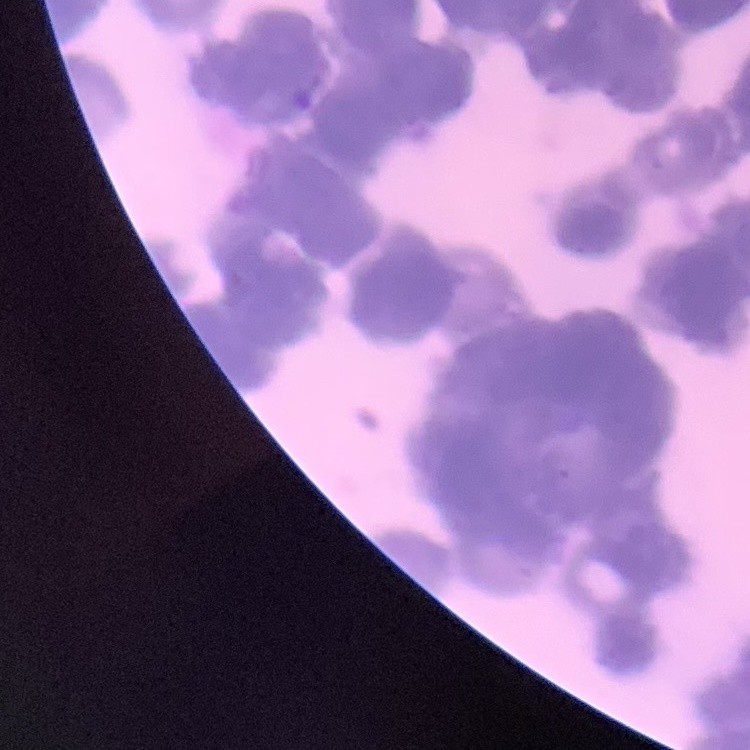

erythrocyte morphology = rouleaux formation
preparation = thin blood smear
stain = Field's or Giemsa
image type = one tile cut from a larger photomicrograph